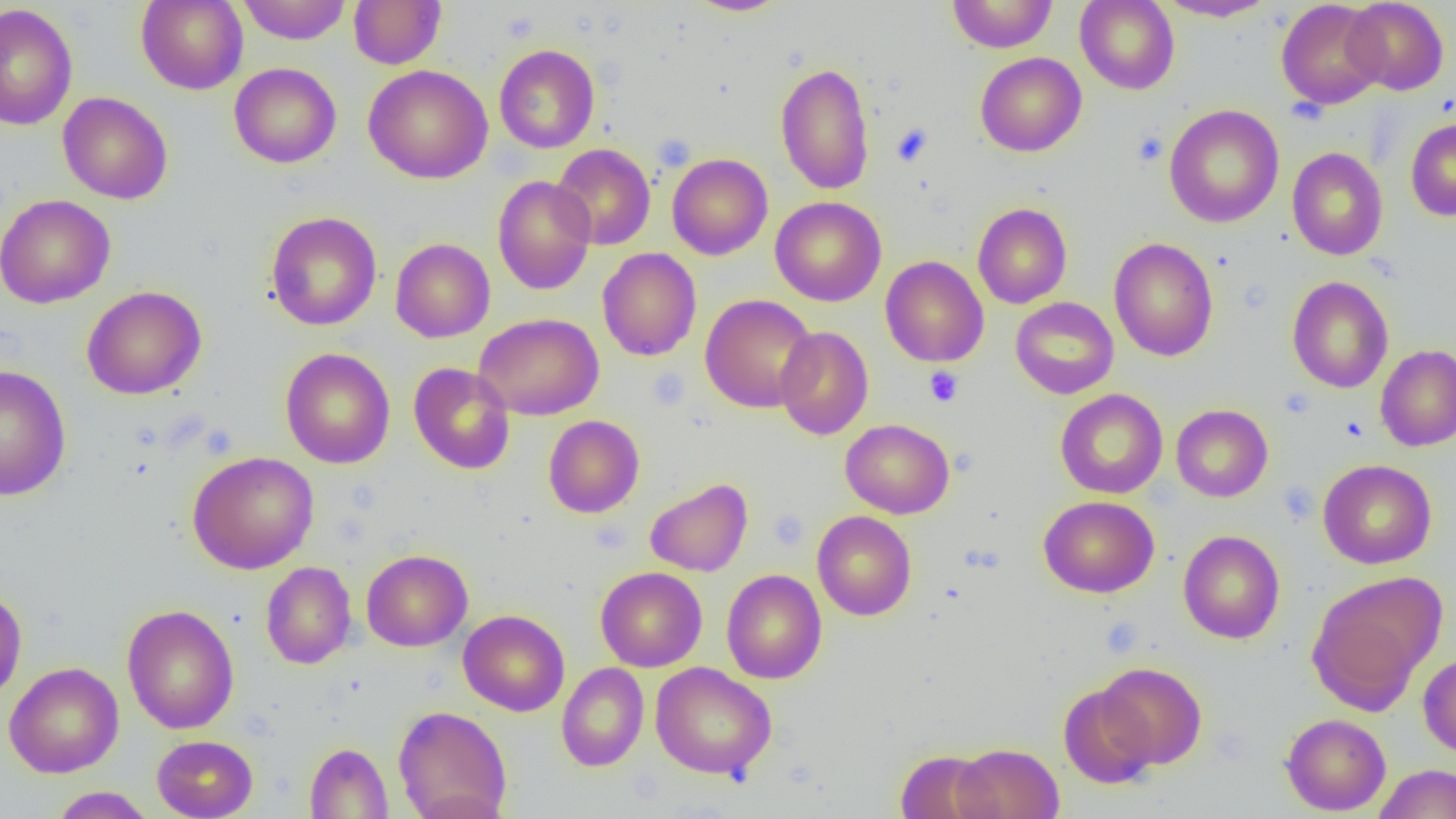
Approximate bounding boxes as named x1/y1/x2/y2 corners in pixels. Uninfected red blood cell locations: (x1=237, y1=0, x2=352, y2=44), (x1=348, y1=0, x2=446, y2=69), (x1=686, y1=0, x2=791, y2=16), (x1=947, y1=0, x2=1057, y2=53), (x1=1075, y1=0, x2=1180, y2=94), (x1=1157, y1=0, x2=1277, y2=21), (x1=1276, y1=0, x2=1386, y2=110), (x1=1343, y1=0, x2=1448, y2=95), (x1=136, y1=1, x2=248, y2=94), (x1=0, y1=3, x2=78, y2=131), (x1=493, y1=44, x2=599, y2=153), (x1=975, y1=52, x2=1086, y2=157), (x1=229, y1=62, x2=341, y2=168), (x1=775, y1=62, x2=875, y2=195), (x1=364, y1=64, x2=493, y2=184), (x1=58, y1=91, x2=173, y2=204), (x1=1164, y1=104, x2=1284, y2=228), (x1=1406, y1=118, x2=1456, y2=221), (x1=551, y1=143, x2=655, y2=250), (x1=1287, y1=147, x2=1388, y2=261), (x1=667, y1=153, x2=773, y2=259), (x1=493, y1=176, x2=596, y2=295), (x1=0, y1=194, x2=115, y2=308), (x1=770, y1=196, x2=886, y2=306), (x1=972, y1=203, x2=1072, y2=308), (x1=265, y1=211, x2=381, y2=331), (x1=1109, y1=237, x2=1219, y2=361), (x1=390, y1=238, x2=495, y2=342), (x1=597, y1=248, x2=701, y2=361), (x1=880, y1=256, x2=989, y2=367), (x1=1286, y1=276, x2=1394, y2=393), (x1=82, y1=285, x2=207, y2=400), (x1=700, y1=294, x2=818, y2=413), (x1=1010, y1=296, x2=1119, y2=399), (x1=475, y1=312, x2=603, y2=420), (x1=774, y1=326, x2=874, y2=440), (x1=1376, y1=344, x2=1456, y2=452), (x1=280, y1=347, x2=395, y2=469), (x1=408, y1=362, x2=515, y2=475), (x1=0, y1=363, x2=72, y2=501), (x1=1055, y1=389, x2=1168, y2=499), (x1=1171, y1=404, x2=1273, y2=502), (x1=543, y1=415, x2=644, y2=518), (x1=841, y1=419, x2=954, y2=519), (x1=187, y1=451, x2=319, y2=574), (x1=1318, y1=459, x2=1437, y2=569), (x1=645, y1=478, x2=753, y2=577), (x1=1039, y1=495, x2=1159, y2=598), (x1=812, y1=511, x2=917, y2=620), (x1=1178, y1=530, x2=1285, y2=644), (x1=361, y1=549, x2=472, y2=651), (x1=261, y1=561, x2=356, y2=669), (x1=596, y1=566, x2=707, y2=672), (x1=722, y1=569, x2=827, y2=684), (x1=1306, y1=573, x2=1444, y2=714), (x1=0, y1=586, x2=27, y2=704), (x1=121, y1=604, x2=239, y2=733), (x1=458, y1=609, x2=570, y2=716), (x1=1418, y1=653, x2=1456, y2=758), (x1=1097, y1=661, x2=1206, y2=769), (x1=4, y1=662, x2=124, y2=778), (x1=557, y1=662, x2=649, y2=771), (x1=650, y1=662, x2=776, y2=780), (x1=1058, y1=684, x2=1157, y2=788), (x1=393, y1=705, x2=512, y2=819), (x1=1281, y1=713, x2=1391, y2=815), (x1=151, y1=735, x2=258, y2=818), (x1=304, y1=743, x2=393, y2=818), (x1=952, y1=743, x2=1063, y2=819), (x1=895, y1=749, x2=996, y2=819), (x1=1373, y1=763, x2=1456, y2=819), (x1=50, y1=786, x2=155, y2=818). Platelet locations: (x1=501, y1=10, x2=539, y2=44), (x1=1286, y1=96, x2=1328, y2=125), (x1=890, y1=123, x2=933, y2=167), (x1=1133, y1=131, x2=1168, y2=167), (x1=649, y1=367, x2=690, y2=411), (x1=924, y1=367, x2=963, y2=406), (x1=1340, y1=417, x2=1367, y2=442), (x1=1278, y1=481, x2=1321, y2=525), (x1=768, y1=509, x2=809, y2=551), (x1=1099, y1=618, x2=1144, y2=657). Slide-level diagnosis: no evidence of blood parasites. Light microscopy. Image is 1456×819 pixels. Thin blood film. Single field of view. Captured at 1000x magnification.